Assess this cell for malaria.
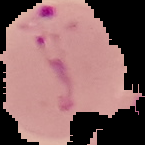
It is parasitized.

From a thin blood smear. Segmented cell region on a black background. Image is 145×145 pixels.